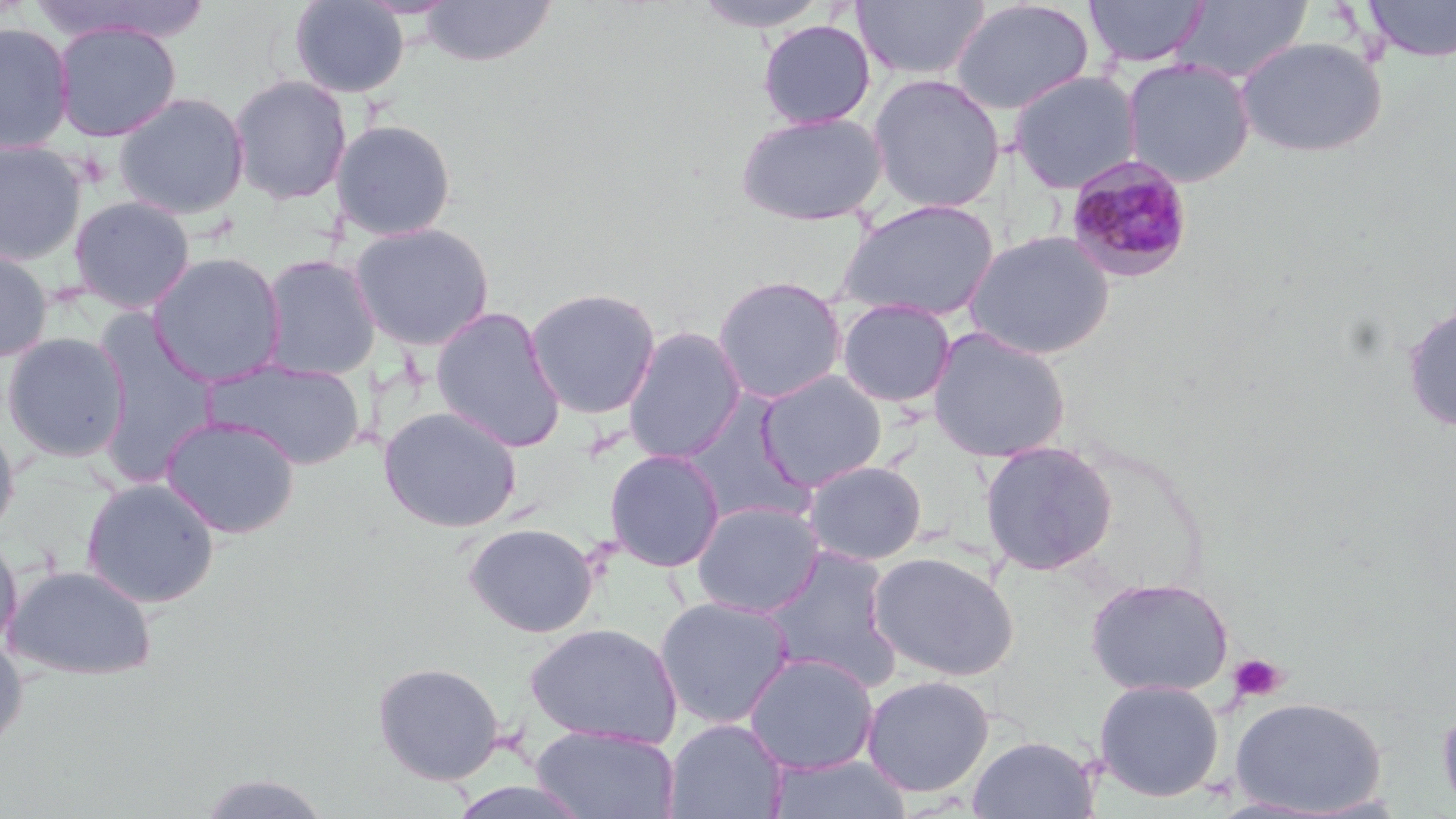

slide-level diagnosis = Plasmodium malariae
image size = 1456×819 pixels
uninfected red blood cell locations = approximate bounding boxes as (x1, y1, x2, y2) in pixels: (290, 0, 410, 98), (420, 0, 558, 67), (690, 0, 835, 32), (853, 0, 991, 82), (1084, 0, 1208, 68), (1173, 0, 1313, 84), (1360, 0, 1456, 62), (948, 1, 1095, 116), (757, 19, 876, 129), (53, 20, 182, 142), (0, 21, 75, 153), (1235, 35, 1387, 158), (1121, 58, 1256, 187), (1008, 71, 1143, 193), (867, 73, 1006, 214), (229, 74, 352, 205), (113, 91, 250, 220), (734, 111, 888, 226), (332, 118, 458, 242), (0, 139, 87, 267), (69, 196, 196, 313), (835, 198, 1000, 323), (349, 221, 495, 351), (964, 228, 1115, 360), (0, 245, 53, 363), (147, 252, 286, 386), (259, 253, 381, 381), (712, 274, 848, 404), (525, 287, 662, 420), (836, 298, 956, 408), (1402, 301, 1456, 433), (430, 305, 566, 452), (92, 313, 219, 481), (622, 326, 747, 463), (927, 327, 1071, 463), (1, 331, 131, 462), (204, 358, 367, 470), (755, 369, 888, 491), (678, 391, 814, 525), (378, 406, 523, 533), (160, 415, 301, 538), (0, 420, 19, 545), (979, 440, 1118, 576), (604, 449, 725, 572), (802, 460, 927, 565), (81, 477, 220, 608), (692, 501, 824, 617), (462, 522, 599, 637), (0, 532, 22, 656), (761, 546, 901, 688), (867, 550, 1020, 682), (3, 563, 157, 679), (1085, 576, 1235, 697), (654, 596, 794, 728), (525, 621, 683, 748), (0, 633, 28, 755), (744, 652, 879, 774), (372, 660, 505, 785), (860, 675, 995, 796), (1093, 678, 1224, 802), (1229, 697, 1386, 815), (1437, 699, 1456, 816), (663, 718, 788, 819), (530, 725, 680, 819), (966, 735, 1100, 818), (766, 753, 914, 819), (195, 771, 334, 818), (442, 778, 595, 819)
stain = May-Grünwald-Giemsa
modality = optical microscopy
platelet locations = approximate bounding boxes as (x1, y1, x2, y2) in pixels: (1228, 653, 1287, 703)
preparation = thin blood film
field of view = single
Plasmodium malariae-infected red blood cell locations = approximate bounding boxes as (x1, y1, x2, y2) in pixels: (1064, 156, 1196, 285)
magnification = 1000x